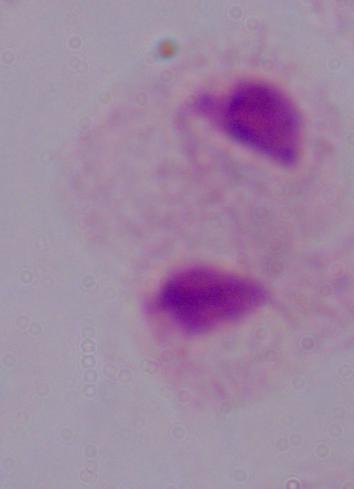 Captured at 1000x magnification. Photomicrograph. A trichomonad is shown.